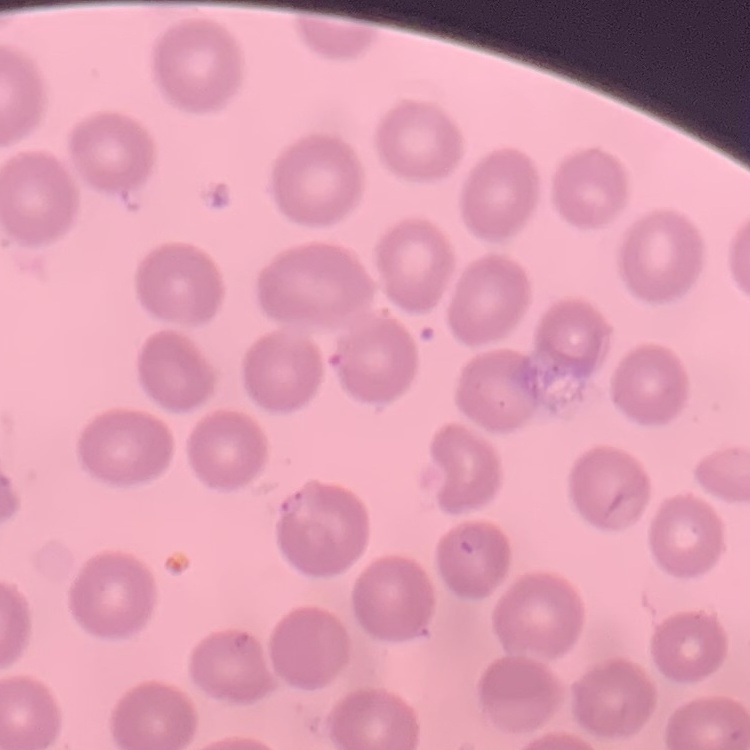
Summary:
  - Red blood cell morphology: no rouleaux formation
  - Preparation: thin blood film
  - Stain: Field's or Giemsa
  - Image type: square crop of a larger photomicrograph